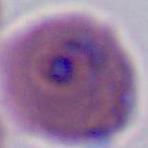

400x or 1000x magnification. Photomicrograph. A Plasmodium parasite is shown.